Locate every leukocyte (white blood cell).
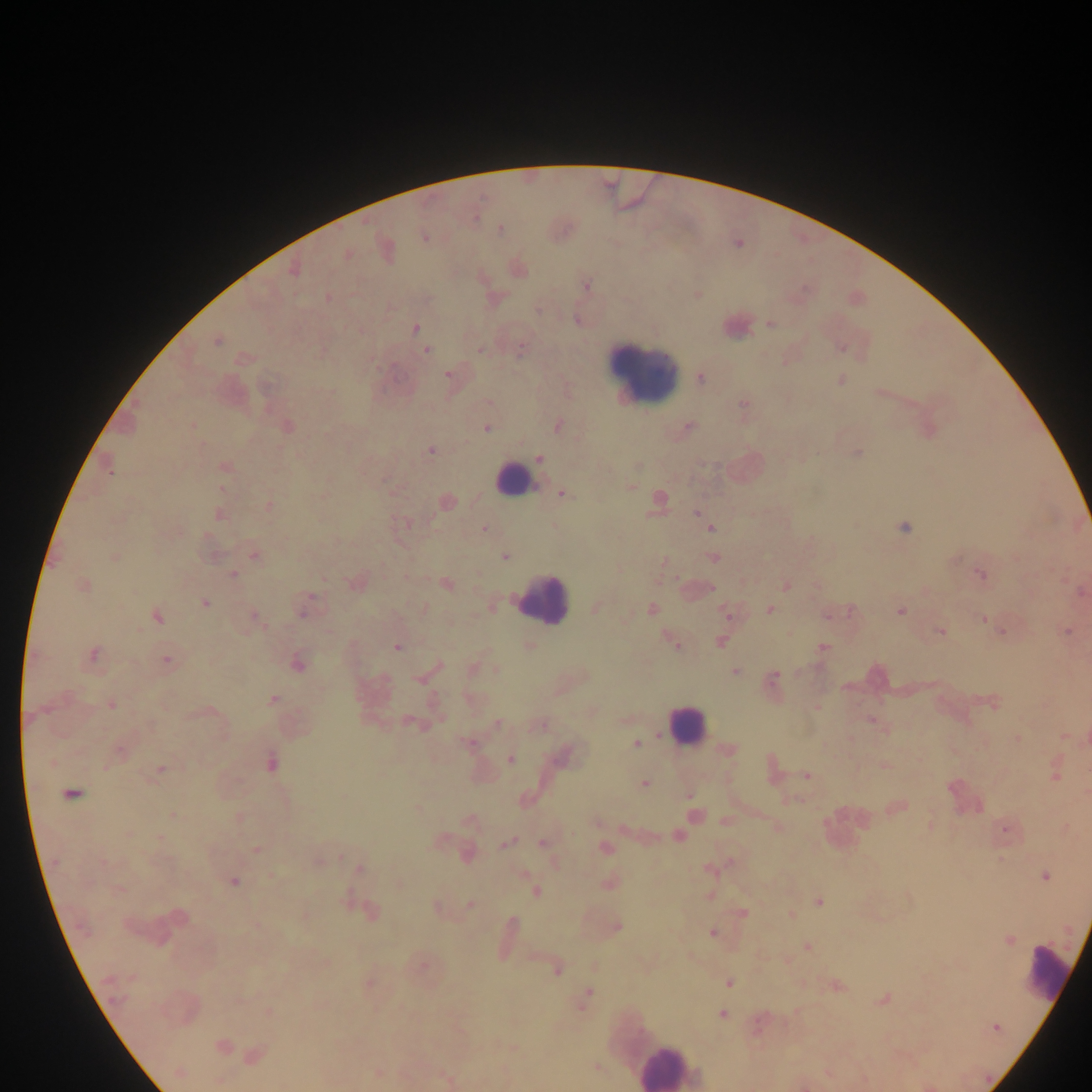
Approximate centers as x y in pixels.
Leukocytes: 735 325; 643 369; 515 480; 542 598; 686 725; 845 828; 1048 974; 668 1066.

Plasmodium parasite locations: 500 229; 424 237; 385 249; 348 254; 518 268; 293 269; 586 285; 698 294; 327 297; 578 320; 770 324; 415 328; 217 340; 841 346; 480 349; 427 350; 243 358; 448 374; 699 377; 841 379; 880 393; 488 402; 743 405; 557 425; 287 426; 487 427; 688 427; 430 450; 856 452; 539 459; 108 466; 224 467; 629 486; 221 488; 562 494; 658 500; 446 501; 268 505; 698 513; 218 514; 403 523; 903 527; 483 528; 711 528; 253 555; 504 555; 114 557; 713 558; 663 561; 981 574; 232 575; 356 581; 445 583; 785 585; 83 586; 696 589; 1081 591; 205 602; 490 605; 303 607; 594 608; 651 609; 769 609; 900 610; 851 611; 727 613; 830 613; 157 616; 254 617; 984 618; 940 630; 1001 630; 1067 631; 789 634; 720 640; 673 641; 530 646; 397 647; 822 648; 91 655; 167 659; 297 663; 473 669; 734 671; 423 675; 772 680; 560 687; 470 698; 272 699; 992 701; 111 705; 816 706; 626 718; 871 719; 413 722; 497 723; 540 725; 1065 735; 1017 739; 468 743; 636 743; 120 750; 728 750; 563 756; 510 759; 270 762; 883 765; 160 769; 772 770; 1056 772; 807 775; 644 783; 71 794; 688 795; 794 799; 897 806; 417 809; 173 815; 694 815; 239 817; 470 821; 595 822; 725 822; 930 824; 778 827; 1005 828; 1066 828; 624 829; 678 836; 159 838; 438 841; 506 843; 542 843; 604 848; 256 849; 465 853; 317 859; 730 862; 555 863; 709 868; 360 869; 1044 875; 233 881; 608 882; 399 883; 535 891; 708 895; 818 902; 470 904; 437 906; 369 911; 742 913; 791 914; 176 917; 616 927; 713 932; 506 936; 1007 939; 807 946; 786 960; 421 964; 556 969; 368 983; 728 983; 835 985; 584 999; 883 999; 270 1012; 721 1013; 758 1026; 993 1027; 221 1046; 513 1048; 254 1054; 596 1067; 179 1072; 378 1073; 447 1080; 219 1081; 927 1085. Single field of view. Photographed through a microscope with a mobile-phone camera. Image is 1092×1092 pixels. Thick blood smear. Collected in Ghana.